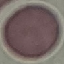

Result: negative for malaria parasites. Acquired by smartphone through the microscope eyepiece. Thin blood film. Giemsa-stained preparation. Cell patch, automatically extracted from a larger field of view and resized to 64 × 64 pixels.